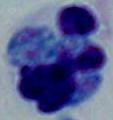

{
  "magnification": "1000x",
  "identification": "white blood cell",
  "modality": "photomicrograph"
}